State which parasite is depicted.
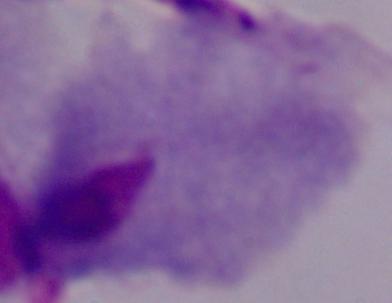
This is a trichomonad.

Summary:
  - Modality: photomicrograph
  - Magnification: 1000x